Assess this cell for malaria.
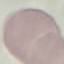

It is uninfected.

Thin smear of blood. Acquired by smartphone through the microscope eyepiece. Giemsa stain. Automatically extracted cell patch, resized to 64 × 64 pixels.